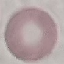
Result: negative for malaria parasites. Giemsa stain. Photographed with a smartphone camera at the microscope eyepiece. Thin blood film. Cell patch, automatically extracted from a larger field of view and resized to 64 × 64 pixels.